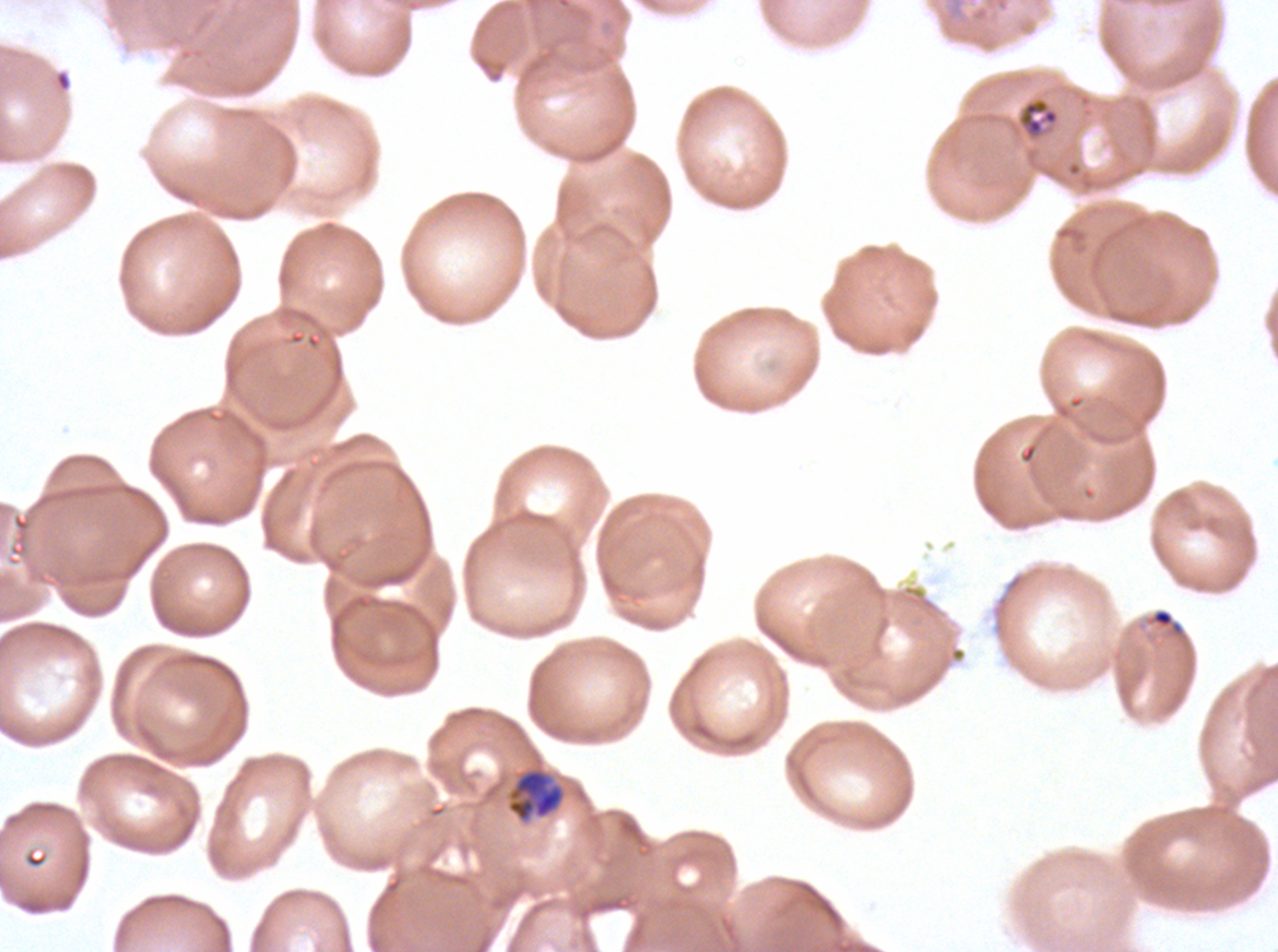
{
  "life_cycle_stages_observed": "ring, late trophozoite",
  "preparation": "thin blood smear",
  "field_of_view": "sub-image separated from a larger composite",
  "late_trophozoite_locations": "approximate bounding rectangles given as corner coordinates in pixels from the top-left: (x1=506, y1=765, x2=567, y2=824)",
  "image_size": "1278×952 pixels",
  "ring_locations": "approximate bounding rectangles given as corner coordinates in pixels from the top-left: (x1=1150, y1=608, x2=1184, y2=635)",
  "stain": "Giemsa",
  "debris_locations": "approximate bounding rectangles given as corner coordinates in pixels from the top-left: (x1=1016, y1=97, x2=1060, y2=140)",
  "specimen": "P. falciparum cultured ex vivo for 24 to 48 hours, from a patient in The Gambia"
}